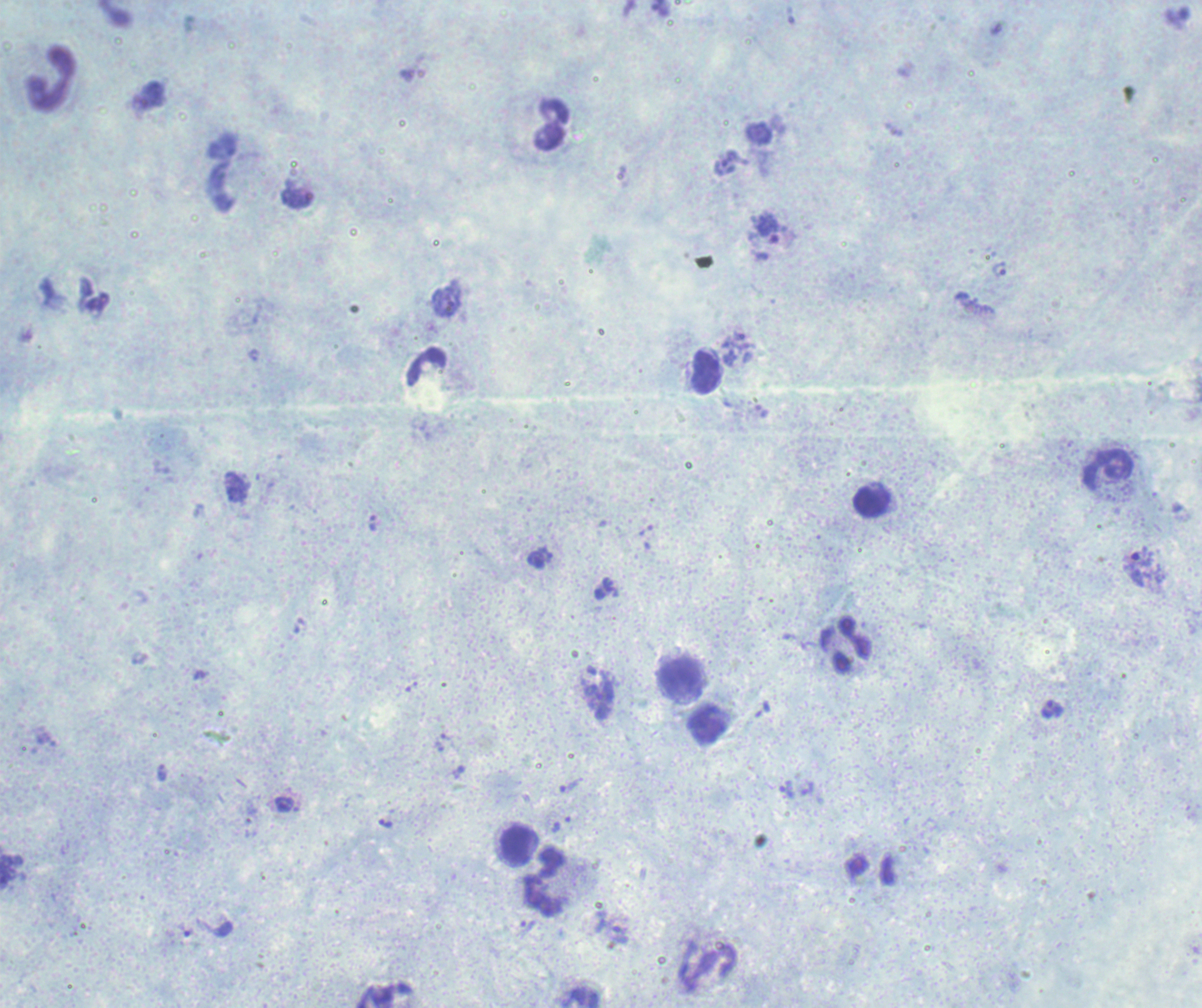
One field from this slide. Romanowsky stain. Thick smear of blood. Image is 1202×1008 pixels.